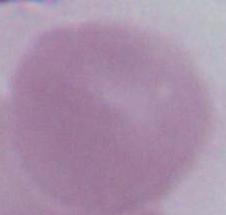

modality = micrograph
identification = erythrocyte
magnification = 1000x